Report the malaria status of this cell.
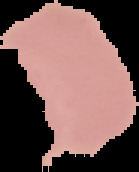
Uninfected.

image size = 139×172 pixels
image type = segmented cell region on a black background
preparation = thin blood smear